State which cell type is depicted.
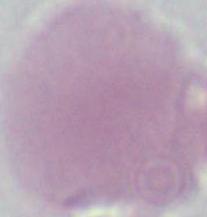
An erythrocyte.

magnification = 1000x
modality = photomicrograph